Give the position of every malaria parasite.
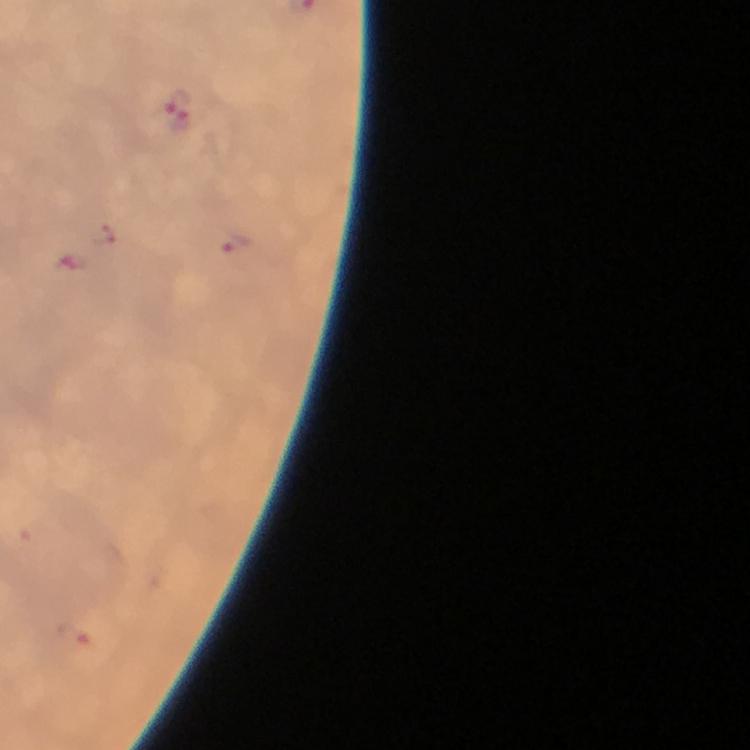
Approximate centers as [x, y] in pixels.
Malaria parasites: [179, 110], [234, 241], [73, 634].

{
  "magnification": "100x",
  "context": "from a diagnostic examination for malaria",
  "preparation": "thick blood film",
  "cropped_from": "one field of view",
  "capture": "smartphone mounted on the microscope",
  "image_size": "750×750 pixels",
  "stain": "Giemsa",
  "immersion_oil": "applied"
}